Locate every malaria parasite and every leukocyte.
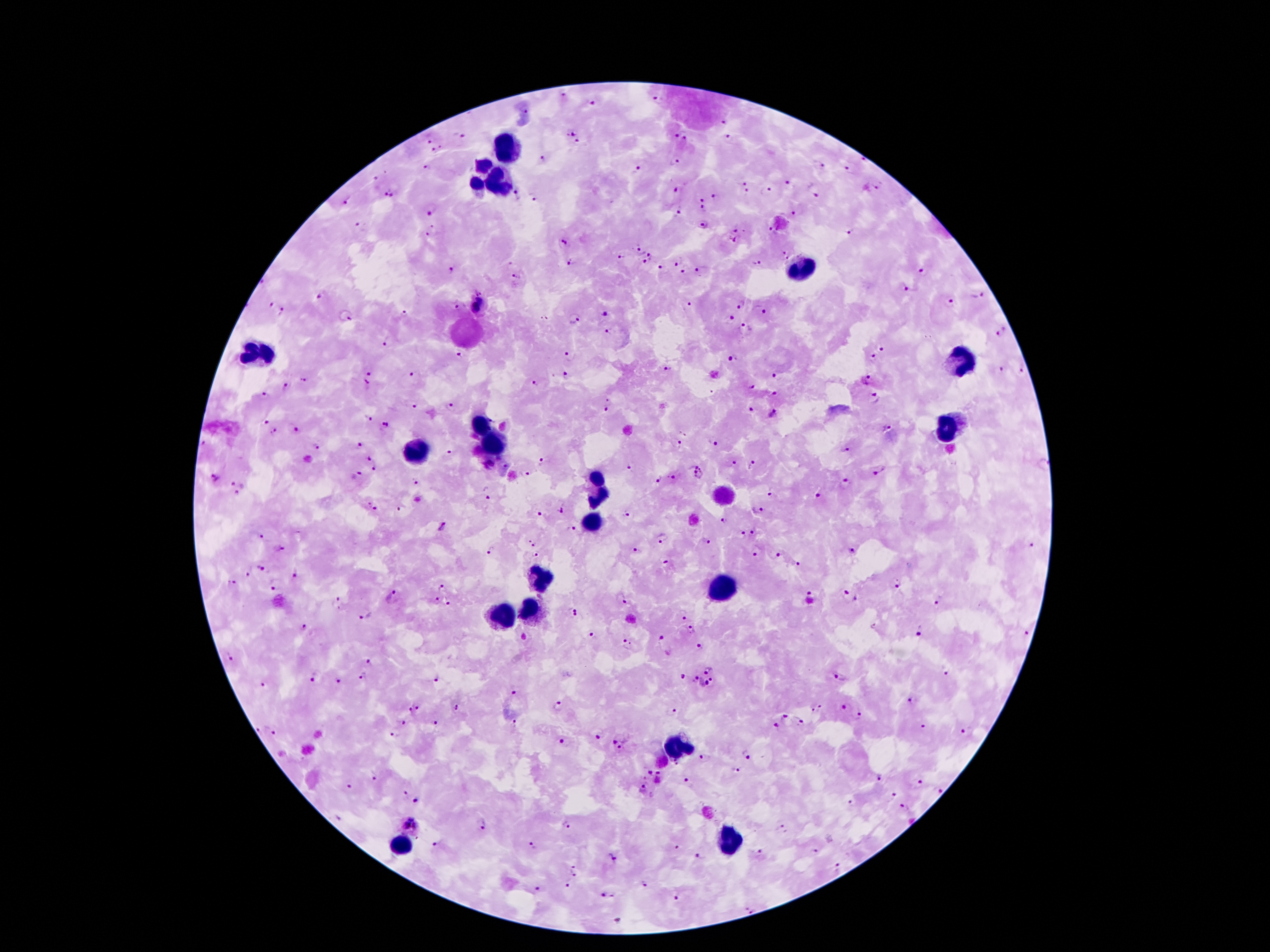

Approximate centers as [x, y] in pixels.
Malaria parasites: [564, 97], [659, 101], [593, 103], [525, 109], [723, 122], [573, 132], [674, 135], [458, 136], [728, 136], [432, 137], [685, 139], [580, 143], [439, 150], [542, 158], [865, 161], [675, 162], [819, 166], [427, 168], [848, 169], [638, 170], [374, 179], [743, 181], [788, 183], [678, 188], [878, 188], [766, 191], [384, 192], [747, 193], [516, 194], [815, 194], [396, 195], [717, 197], [533, 198], [703, 200], [346, 202], [432, 210], [704, 210], [676, 214], [795, 214], [360, 225], [703, 226], [737, 229], [432, 230], [772, 230], [847, 231], [733, 239], [562, 240], [640, 251], [782, 254], [621, 255], [653, 256], [678, 261], [572, 263], [644, 263], [756, 263], [510, 264], [452, 269], [665, 269], [685, 272], [703, 272], [921, 272], [516, 277], [908, 286], [478, 289], [976, 295], [321, 297], [480, 301], [950, 302], [270, 304], [690, 304], [740, 304], [461, 307], [475, 308], [761, 310], [283, 311], [405, 312], [605, 313], [344, 315], [731, 317], [576, 318], [543, 319], [748, 329], [612, 331], [1002, 331], [387, 342], [882, 347], [458, 355], [872, 356], [568, 357], [732, 358], [667, 368], [1022, 368], [1000, 369], [368, 370], [414, 374], [777, 376], [565, 377], [303, 380], [867, 380], [537, 383], [368, 384], [751, 387], [287, 388], [774, 394], [264, 395], [875, 399], [607, 404], [412, 405], [451, 406], [750, 411], [774, 413], [368, 419], [265, 420], [385, 425], [887, 427], [296, 429], [275, 432], [713, 442], [676, 444], [203, 445], [316, 446], [361, 446], [846, 450], [450, 453], [368, 459], [542, 462], [735, 462], [754, 464], [505, 465], [630, 465], [374, 468], [880, 470], [698, 471], [360, 473], [528, 474], [214, 477], [673, 478], [658, 479], [415, 481], [230, 484], [845, 484], [486, 493], [238, 495], [770, 495], [819, 496], [367, 504], [761, 508], [399, 509], [376, 510], [562, 510], [540, 512], [626, 514], [723, 522], [441, 528], [571, 529], [741, 532], [754, 532], [262, 537], [663, 539], [532, 542], [709, 542], [1033, 546], [279, 549], [854, 550], [492, 551], [639, 552], [538, 554], [753, 554], [777, 554], [667, 563], [797, 563], [261, 568], [248, 570], [296, 575], [232, 581], [275, 585], [442, 585], [898, 585], [810, 591], [845, 593], [393, 597], [622, 598], [856, 599], [438, 600], [337, 602], [448, 602], [939, 602], [570, 608], [365, 614], [682, 616], [579, 617], [304, 626], [692, 630], [920, 632], [1028, 632], [592, 636], [663, 638], [626, 645], [700, 646], [231, 658], [368, 662], [709, 669], [947, 672], [682, 676], [362, 677], [840, 678], [311, 679], [437, 679], [694, 679], [338, 680], [712, 680], [703, 683], [263, 684], [514, 694], [910, 701], [557, 705], [418, 707], [456, 707], [846, 708], [818, 709], [409, 710], [673, 711], [858, 716], [788, 717], [514, 721], [401, 722], [434, 722], [802, 722], [924, 726], [776, 727], [260, 730], [275, 731], [964, 731], [394, 734], [598, 737], [561, 740], [615, 740], [620, 749], [745, 754], [703, 758], [738, 771], [648, 772], [373, 776], [659, 777], [878, 778], [688, 782], [920, 782], [351, 787], [941, 789], [642, 790], [894, 794], [403, 795], [415, 801], [851, 802], [903, 804], [338, 817], [412, 817], [406, 824], [566, 824], [484, 826], [418, 827], [782, 828], [417, 839], [437, 843], [532, 846], [676, 846], [815, 851], [760, 853], [700, 857], [612, 859], [573, 867], [837, 868], [574, 874], [643, 885], [567, 886], [537, 889], [604, 895], [676, 898], [750, 909], [619, 920].
Leukocytes: [511, 149], [484, 164], [477, 180], [498, 180], [802, 267], [259, 353], [959, 362], [482, 425], [952, 428], [493, 442], [416, 451], [596, 487], [591, 523], [541, 580], [725, 591], [528, 612], [502, 616], [678, 746], [730, 839], [401, 844].

capture = smartphone through the microscope eyepiece
stain = Giemsa
magnification = 100x
patient malaria status = infected with Plasmodium falciparum
image size = 1270×952 pixels
preparation = thick blood smear
field of view = one from this slide